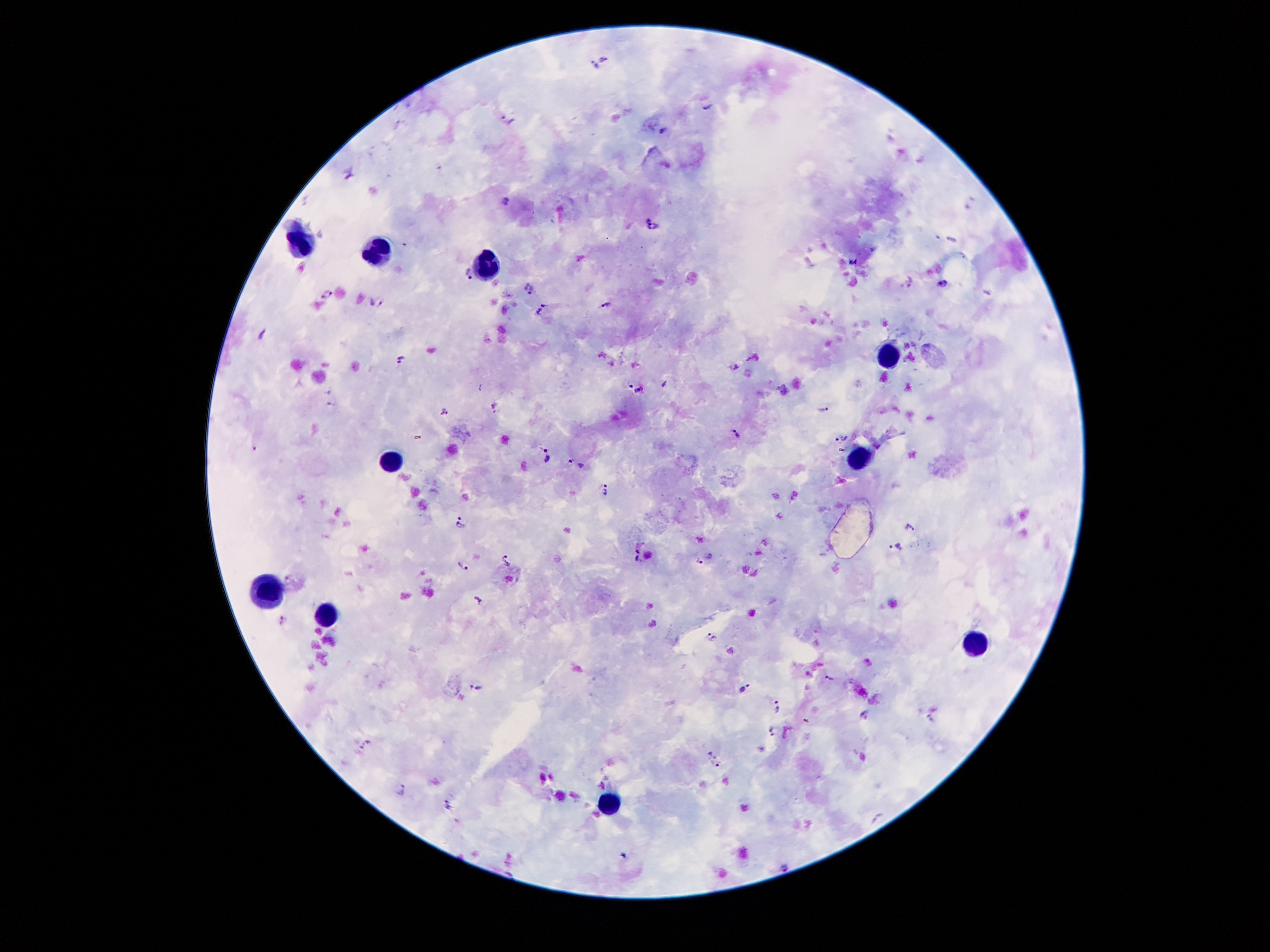
malaria_parasite_locations: 'approximate centers as {x, y} in pixels: {604, 59}, {594, 66}, {708, 106}, {507, 119}, {663, 131}, {351, 172}, {505, 200}, {654, 225}, {853, 260}, {302, 268}, {468, 274}, {943, 285}, {528, 288}, {327, 294}, {375, 302}, {606, 303}, {541, 309}, {263, 330}, {753, 358}, {401, 360}, {734, 367}, {629, 384}, {482, 387}, {639, 391}, {494, 406}, {823, 408}, {444, 409}, {737, 432}, {844, 439}, {255, 447}, {547, 457}, {570, 462}, {582, 466}, {605, 489}, {459, 523}, {910, 524}, {638, 546}, {897, 547}, {507, 559}, {638, 561}, {700, 561}, {462, 563}, {286, 578}, {479, 597}, {282, 620}, {711, 637}, {829, 677}, {477, 687}, {743, 689}, {777, 708}, {864, 713}, {806, 720}, {771, 728}, {366, 745}, {714, 761}, {400, 788}, {450, 804}, {784, 864}'
preparation: thick blood smear
capture: smartphone camera through the microscope eyepiece
leukocyte_locations: 'approximate centers as {x, y} in pixels: {298, 245}, {377, 250}, {486, 260}, {891, 350}, {856, 456}, {391, 458}, {264, 586}, {326, 619}, {975, 642}, {610, 801}'
patient_malaria_status: positive for Plasmodium falciparum
stain: Giemsa
magnification: 100x
field_of_view: single
image_size: 1270×952 pixels